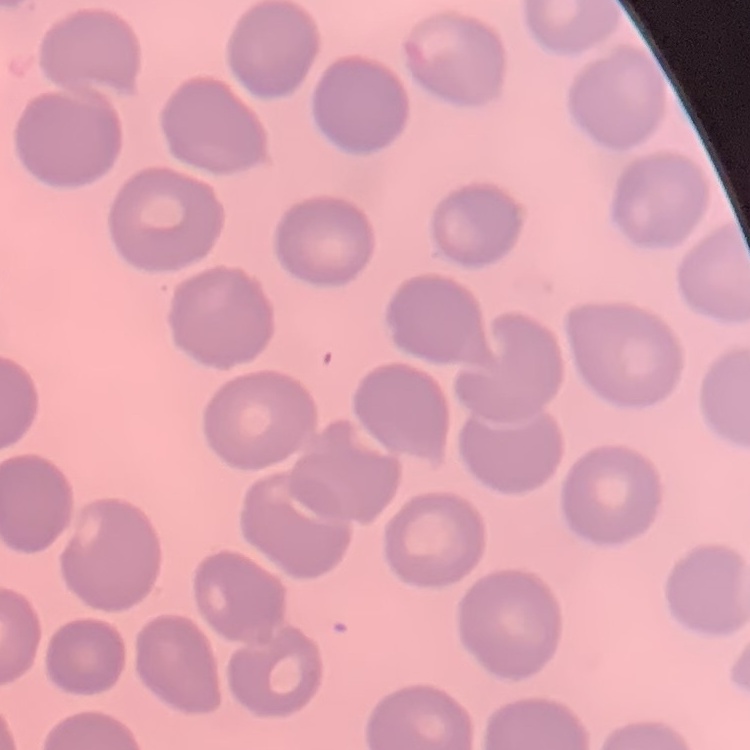

erythrocyte morphology = no rouleaux formation
image type = one tile cut from a larger photomicrograph
stain = Field's or Giemsa
preparation = thin blood film